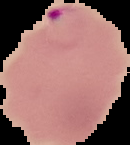

Summary:
  - Image type: segmented cell region with the area outside set to black
  - Malaria status: parasitized
  - Image size: 130×145 pixels
  - Preparation: thin blood smear